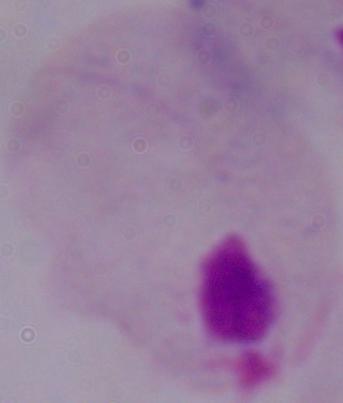

{
  "identification": "trichomonad",
  "modality": "micrograph",
  "magnification": "1000x"
}